Assess this cell for malaria.
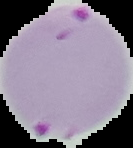

It is parasitized.

Image is 133×148 pixels. From a thin blood film. Cell region segmented out of the field of view; the surrounding area is masked to black.